Assess this cell for malaria.
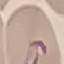
Parasitized.

Summary:
  - Stain: Giemsa
  - Preparation: thin blood smear
  - Capture: smartphone through the microscope eyepiece
  - Image type: cell patch, automatically extracted from a larger field of view and resized to 64 × 64 pixels